Classify this cell by malaria status.
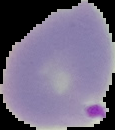
Parasitized.

Summary:
  - Preparation: thin blood smear
  - Image size: 115×130 pixels
  - Image type: segmented cell region on a black background